Locate every Plasmodium parasite.
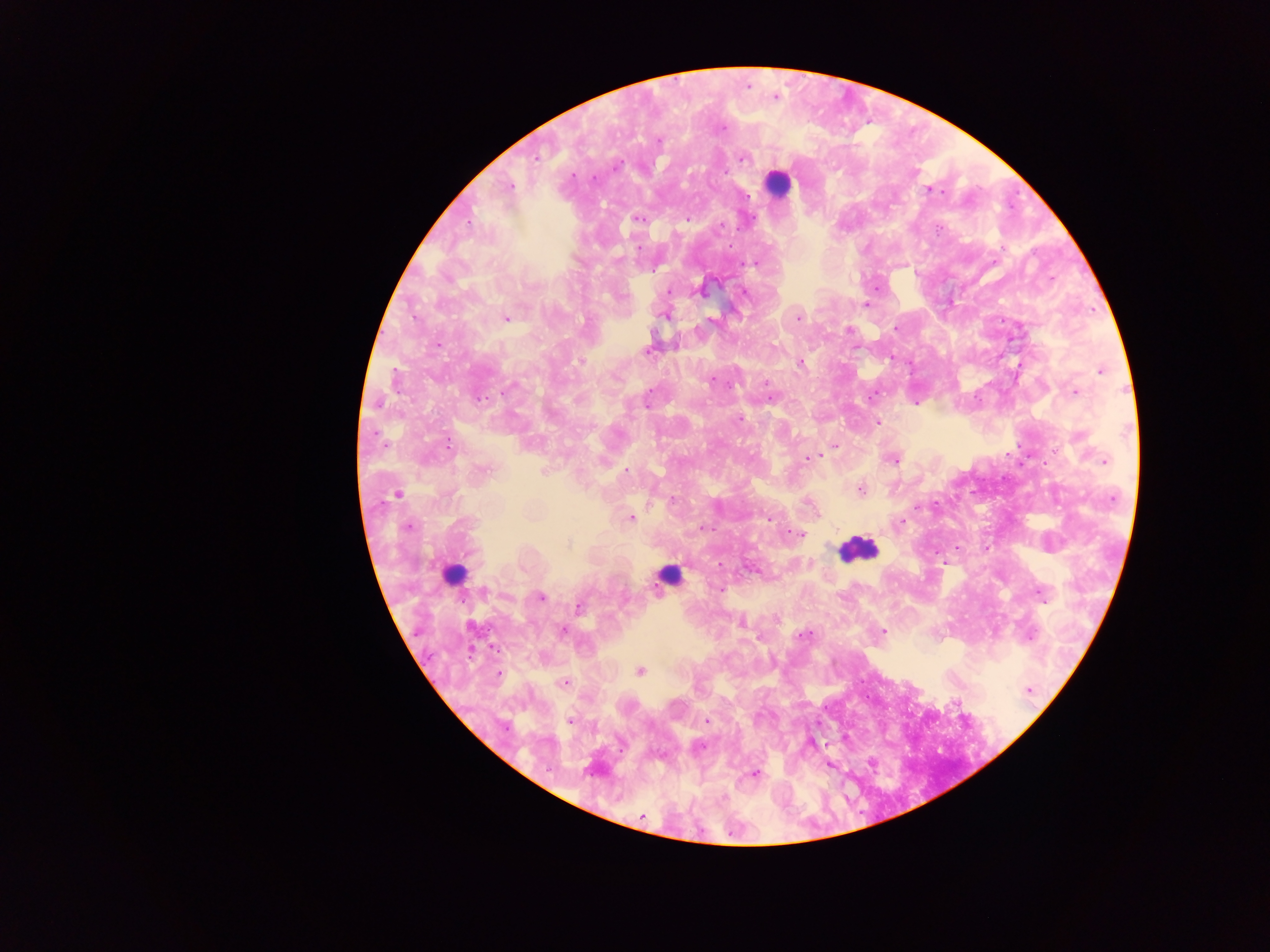
Approximate centers as (x, y) in pixels.
Plasmodium parasites: (776, 97), (724, 128), (658, 141), (536, 157), (743, 158), (617, 165), (725, 172), (593, 178), (510, 186), (930, 190), (747, 195), (638, 219), (687, 219), (468, 223), (720, 225), (638, 247), (755, 263), (668, 291), (700, 292), (745, 293), (866, 304), (664, 316), (505, 318), (798, 318), (710, 320), (895, 329), (849, 330), (438, 344), (648, 351), (580, 361), (800, 363), (1101, 371), (712, 380), (767, 384), (509, 389), (1074, 392), (771, 398), (481, 399), (647, 399), (916, 402), (740, 420), (877, 422), (1079, 437), (834, 445), (808, 457), (894, 460), (1104, 461), (483, 471), (626, 471), (861, 490), (397, 494), (1113, 499), (673, 500), (918, 507), (631, 518), (768, 518), (902, 522), (408, 526), (705, 528), (798, 534), (568, 543), (719, 589), (484, 591), (1042, 593), (541, 597), (579, 608), (741, 623), (563, 631), (882, 631), (803, 635), (1030, 636), (640, 670), (499, 674), (564, 682), (1029, 690), (570, 721), (707, 721), (700, 747), (756, 774), (642, 816).

Leukocyte locations: (778, 183), (857, 549), (453, 574), (669, 575). One field of view. Image is 1270×952 pixels. Sample from Ghana. Photographed through a microscope with a mobile-phone camera. Thick blood film.